Report the malaria status of this cell.
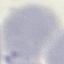

Uninfected.

Summary:
  - Preparation: thin blood smear
  - Image type: cell patch, automatically extracted from a larger field of view and resized to 64 × 64 pixels
  - Capture: smartphone camera at the microscope eyepiece
  - Stain: Giemsa